Give the position of every Plasmodium parasite visible.
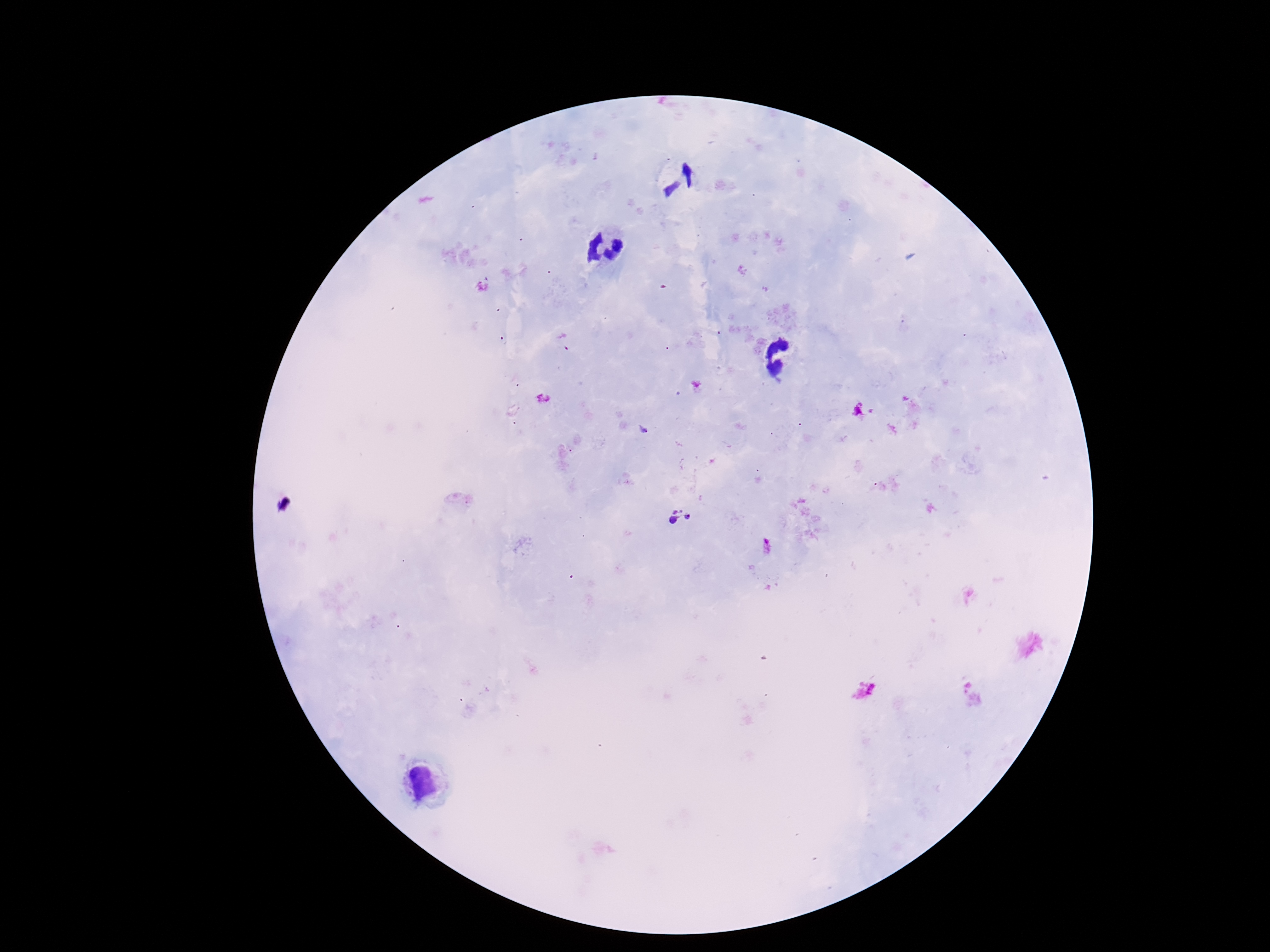
Approximate centers as (x, y) in pixels.
Plasmodium parasites: (680, 518).

Summary:
  - Patient malaria status: positive
  - Magnification: 100x
  - Preparation: thick blood film
  - Field of view: one from this slide
  - Stain: Giemsa
  - Capture: smartphone camera through the microscope eyepiece
  - Image size: 1270×952 pixels